Name the cell type shown.
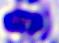

A leukocyte.

modality: micrograph
magnification: 400x